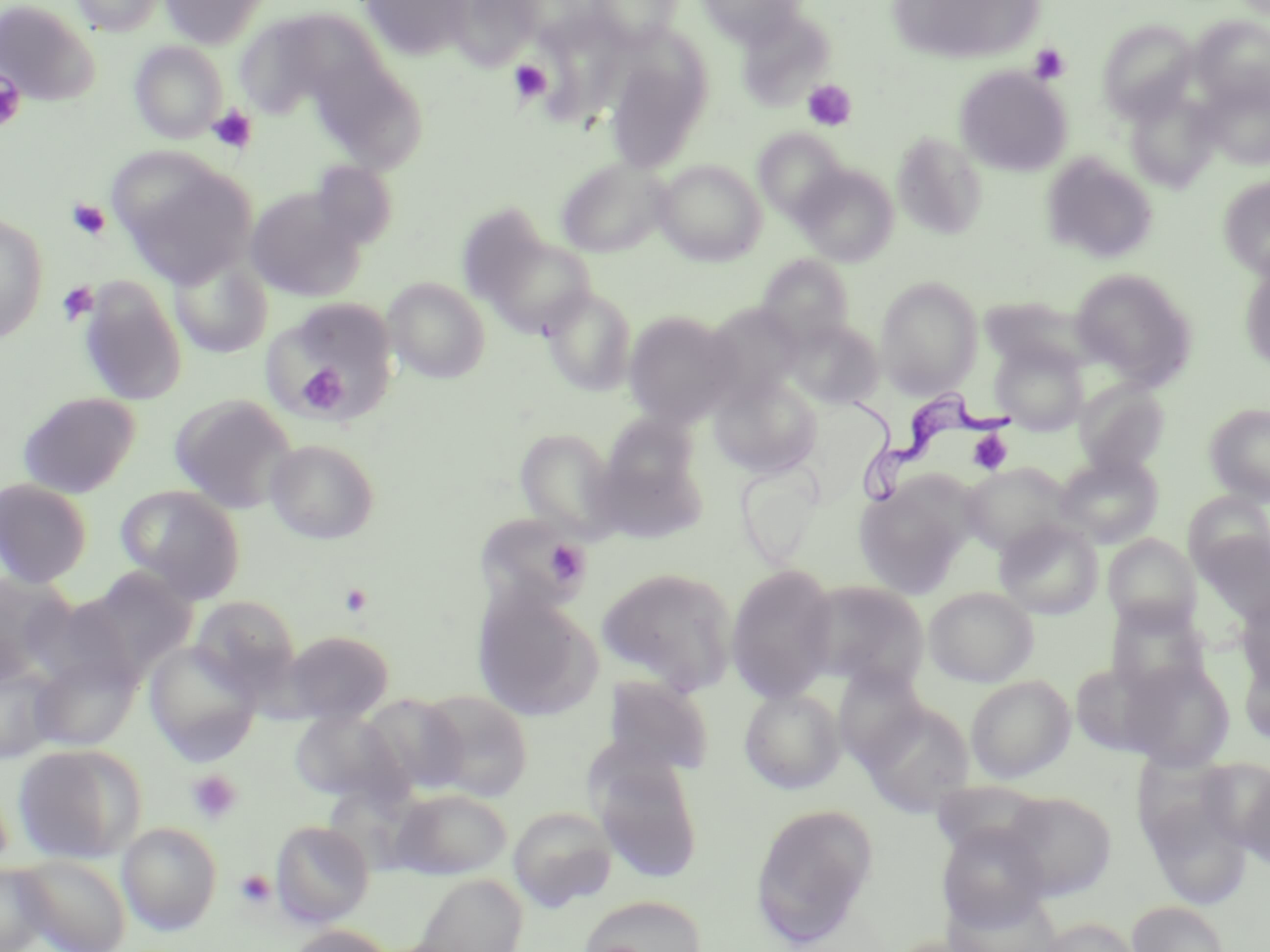

Summary:
  - Coordinate format: approximate bounding boxes as [x1, y1, x2, y2] in pixels
  - Uninfected red blood cell locations: [70, 0, 164, 36], [159, 0, 270, 49], [358, 0, 473, 62], [514, 0, 604, 50], [586, 0, 682, 49], [695, 0, 806, 46], [0, 1, 99, 105], [449, 1, 542, 69], [885, 1, 1047, 64], [283, 8, 389, 98], [734, 9, 835, 111], [1190, 16, 1270, 110], [237, 20, 312, 114], [1097, 20, 1200, 122], [129, 40, 227, 144], [317, 55, 412, 146], [606, 56, 710, 172], [956, 66, 1072, 176], [1198, 77, 1270, 170], [1124, 88, 1221, 191], [753, 128, 847, 222], [892, 132, 988, 240], [1041, 153, 1158, 263], [556, 157, 671, 257], [120, 160, 258, 287], [307, 160, 397, 253], [653, 160, 766, 266], [794, 164, 898, 265], [1218, 176, 1270, 281], [243, 186, 366, 301], [0, 215, 48, 343], [477, 231, 598, 338], [169, 253, 273, 358], [755, 254, 856, 348], [1239, 259, 1270, 373], [1069, 268, 1197, 386], [876, 275, 983, 397], [383, 277, 491, 384], [78, 278, 187, 406], [541, 286, 638, 396], [270, 297, 399, 417], [703, 304, 805, 402], [623, 310, 741, 427], [785, 318, 884, 410], [990, 340, 1089, 436], [709, 375, 822, 478], [1074, 380, 1170, 476], [18, 392, 141, 498], [169, 394, 298, 514], [1205, 403, 1270, 506], [600, 412, 704, 506], [514, 427, 620, 538], [265, 439, 380, 544], [1053, 453, 1164, 549], [734, 461, 825, 568], [960, 462, 1074, 556], [0, 479, 92, 587], [854, 479, 972, 598], [116, 486, 246, 603], [1184, 492, 1270, 577], [478, 515, 591, 614], [993, 517, 1103, 620], [1196, 530, 1270, 624], [1102, 533, 1201, 633], [726, 564, 839, 704], [87, 565, 198, 675], [597, 566, 739, 694], [0, 573, 73, 684], [800, 579, 929, 692], [471, 585, 604, 723], [924, 587, 1039, 687], [1236, 591, 1270, 697], [29, 593, 145, 695], [190, 596, 301, 699], [1105, 601, 1212, 700], [283, 630, 395, 725], [145, 641, 261, 763], [1238, 647, 1270, 751], [30, 652, 140, 751], [1119, 658, 1235, 772], [1070, 659, 1176, 757], [0, 661, 62, 763], [832, 665, 931, 772], [601, 674, 714, 777], [966, 675, 1075, 782], [739, 688, 846, 794], [417, 690, 534, 801], [360, 693, 469, 795], [858, 700, 977, 817], [290, 711, 407, 804], [12, 743, 146, 863], [590, 754, 703, 883], [1198, 757, 1270, 856], [1235, 764, 1270, 869], [1140, 786, 1253, 908], [390, 788, 513, 880], [1001, 790, 1117, 900], [751, 803, 879, 946], [509, 807, 617, 911], [270, 820, 375, 927], [118, 821, 222, 935], [936, 821, 1051, 933], [15, 853, 132, 952], [0, 862, 52, 952], [411, 872, 528, 952], [578, 895, 708, 952], [1128, 901, 1231, 952], [1037, 917, 1142, 952], [285, 924, 397, 952]
  - Trypanosoma brucei locations: [845, 384, 1014, 501]
  - Platelet locations: [1028, 43, 1070, 84], [508, 59, 552, 106], [0, 69, 27, 133], [802, 80, 856, 131], [208, 105, 257, 154], [67, 199, 111, 240], [58, 281, 98, 325], [298, 365, 349, 415], [968, 430, 1015, 475], [545, 539, 591, 585], [186, 769, 244, 824], [235, 870, 276, 909]
  - Slide-level diagnosis: Trypanosoma brucei
  - Image size: 1270×952 pixels
  - Modality: optical microscopy
  - Field of view: single
  - Stain: May-Grünwald-Giemsa
  - Magnification: 1000x
  - Preparation: thin blood film